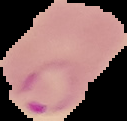
Cell region segmented out of the field of view; the surrounding area is masked to black. Image is 127×121 pixels. Result: malaria parasites detected. From a thin blood smear.